State which parasite is depicted.
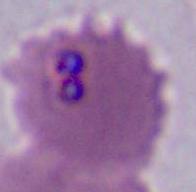
Plasmodium.

Summary:
  - Magnification: 400x or 1000x
  - Modality: photomicrograph